Outline each Trypanosoma brucei.
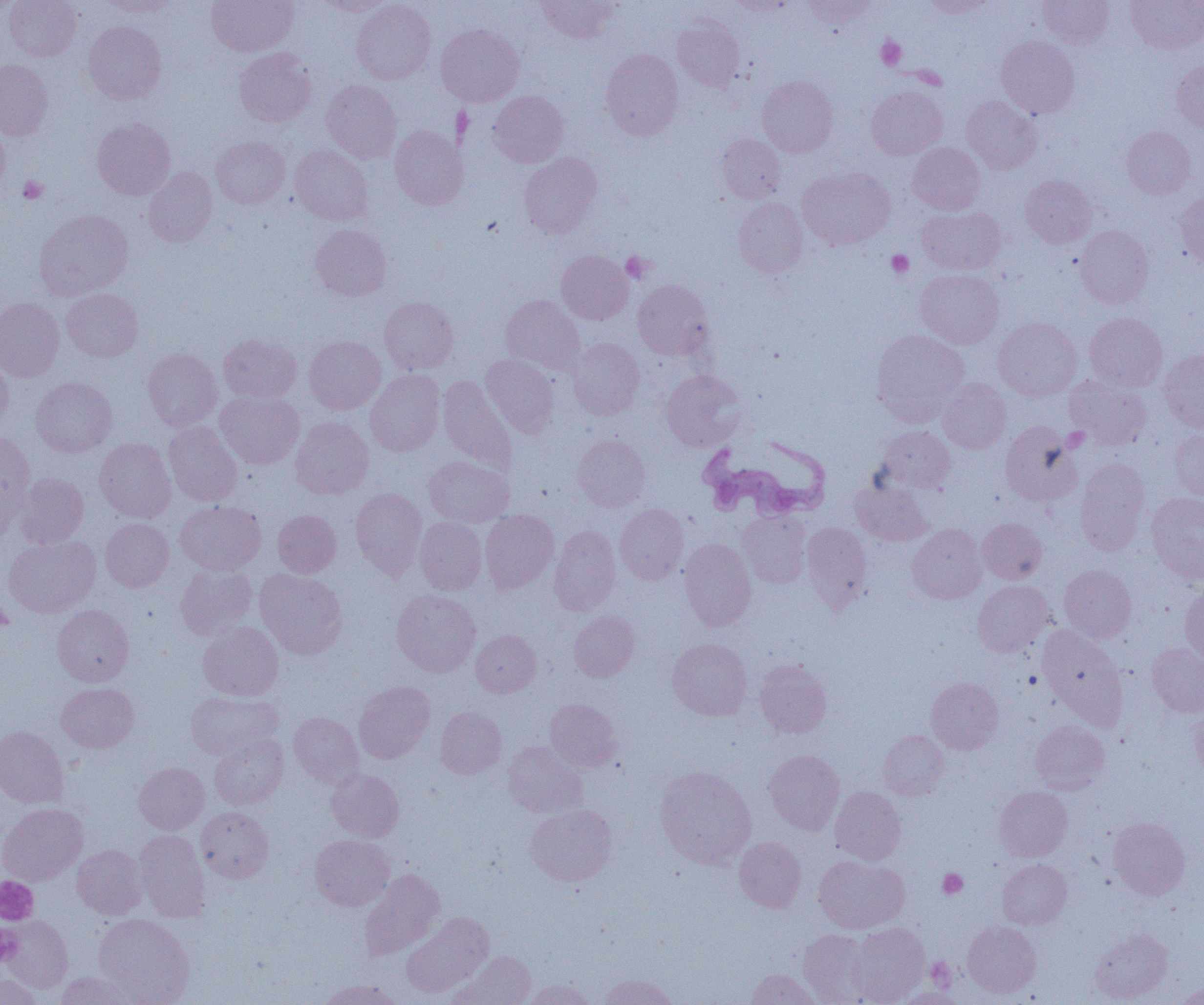

Approximate bounding boxes as named x1/y1/x2/y2 corners in pixels.
Trypanosoma brucei: (x1=698, y1=434, x2=830, y2=523).

Summary:
  - Platelet locations: (x1=877, y1=37, x2=906, y2=70), (x1=19, y1=175, x2=48, y2=203), (x1=886, y1=250, x2=913, y2=277), (x1=622, y1=252, x2=654, y2=283), (x1=938, y1=868, x2=967, y2=899), (x1=0, y1=877, x2=37, y2=923), (x1=0, y1=926, x2=22, y2=965), (x1=925, y1=957, x2=956, y2=990)
  - Uninfected red blood cell locations: (x1=4, y1=0, x2=80, y2=61), (x1=206, y1=0, x2=299, y2=56), (x1=316, y1=0, x2=395, y2=16), (x1=351, y1=0, x2=435, y2=85), (x1=535, y1=0, x2=619, y2=42), (x1=726, y1=0, x2=796, y2=17), (x1=802, y1=0, x2=877, y2=28), (x1=919, y1=0, x2=995, y2=18), (x1=1037, y1=0, x2=1114, y2=48), (x1=1126, y1=0, x2=1204, y2=53), (x1=0, y1=1, x2=17, y2=18), (x1=98, y1=1, x2=181, y2=16), (x1=672, y1=17, x2=744, y2=91), (x1=83, y1=21, x2=167, y2=105), (x1=436, y1=24, x2=524, y2=106), (x1=996, y1=35, x2=1079, y2=118), (x1=234, y1=47, x2=316, y2=127), (x1=600, y1=49, x2=683, y2=140), (x1=0, y1=59, x2=54, y2=140), (x1=1172, y1=60, x2=1204, y2=131), (x1=757, y1=75, x2=838, y2=157), (x1=322, y1=80, x2=402, y2=163), (x1=866, y1=86, x2=948, y2=159), (x1=488, y1=90, x2=568, y2=167), (x1=962, y1=96, x2=1042, y2=173), (x1=92, y1=118, x2=175, y2=200), (x1=0, y1=119, x2=10, y2=194), (x1=390, y1=126, x2=468, y2=210), (x1=1122, y1=126, x2=1196, y2=198), (x1=717, y1=133, x2=786, y2=203), (x1=211, y1=136, x2=290, y2=209), (x1=908, y1=143, x2=985, y2=214), (x1=290, y1=144, x2=373, y2=225), (x1=519, y1=152, x2=602, y2=238), (x1=143, y1=167, x2=217, y2=247), (x1=797, y1=167, x2=895, y2=249), (x1=1020, y1=175, x2=1096, y2=247), (x1=1176, y1=192, x2=1204, y2=269), (x1=733, y1=197, x2=808, y2=277), (x1=917, y1=206, x2=1006, y2=275), (x1=35, y1=209, x2=133, y2=300), (x1=310, y1=224, x2=391, y2=300), (x1=1075, y1=225, x2=1153, y2=308), (x1=556, y1=251, x2=633, y2=324), (x1=915, y1=269, x2=1003, y2=348), (x1=633, y1=279, x2=714, y2=360), (x1=61, y1=288, x2=143, y2=361), (x1=501, y1=295, x2=585, y2=376), (x1=379, y1=297, x2=459, y2=374), (x1=0, y1=298, x2=65, y2=381), (x1=1085, y1=313, x2=1167, y2=392), (x1=993, y1=317, x2=1081, y2=401), (x1=872, y1=330, x2=968, y2=423), (x1=218, y1=334, x2=301, y2=403), (x1=304, y1=335, x2=385, y2=414), (x1=567, y1=337, x2=645, y2=419), (x1=143, y1=348, x2=222, y2=431), (x1=1158, y1=349, x2=1204, y2=433), (x1=481, y1=354, x2=559, y2=438), (x1=0, y1=355, x2=13, y2=431), (x1=366, y1=369, x2=445, y2=456), (x1=661, y1=369, x2=745, y2=451), (x1=1065, y1=375, x2=1152, y2=450), (x1=438, y1=376, x2=517, y2=474), (x1=30, y1=377, x2=117, y2=457), (x1=937, y1=378, x2=1011, y2=454), (x1=215, y1=391, x2=305, y2=468), (x1=291, y1=416, x2=374, y2=499), (x1=164, y1=420, x2=242, y2=507), (x1=1000, y1=421, x2=1082, y2=506), (x1=877, y1=426, x2=956, y2=493), (x1=1170, y1=429, x2=1204, y2=502), (x1=0, y1=432, x2=35, y2=527), (x1=572, y1=434, x2=650, y2=511), (x1=94, y1=438, x2=176, y2=522), (x1=424, y1=456, x2=514, y2=527), (x1=1075, y1=459, x2=1151, y2=555), (x1=15, y1=473, x2=89, y2=548), (x1=852, y1=480, x2=932, y2=546), (x1=350, y1=487, x2=427, y2=580), (x1=1146, y1=492, x2=1204, y2=582), (x1=175, y1=501, x2=266, y2=575), (x1=615, y1=504, x2=689, y2=584), (x1=273, y1=510, x2=341, y2=577), (x1=480, y1=510, x2=559, y2=593), (x1=738, y1=511, x2=811, y2=587), (x1=415, y1=517, x2=487, y2=595), (x1=101, y1=518, x2=174, y2=591), (x1=977, y1=518, x2=1047, y2=584), (x1=801, y1=522, x2=872, y2=611), (x1=907, y1=524, x2=987, y2=604), (x1=549, y1=526, x2=621, y2=615), (x1=4, y1=535, x2=100, y2=618), (x1=678, y1=538, x2=756, y2=630), (x1=175, y1=563, x2=257, y2=639), (x1=1059, y1=565, x2=1136, y2=642), (x1=255, y1=568, x2=348, y2=659), (x1=972, y1=580, x2=1055, y2=657), (x1=1180, y1=586, x2=1204, y2=661), (x1=392, y1=589, x2=481, y2=676), (x1=53, y1=605, x2=133, y2=687), (x1=568, y1=611, x2=640, y2=682), (x1=198, y1=622, x2=284, y2=701), (x1=1038, y1=626, x2=1124, y2=719), (x1=471, y1=630, x2=541, y2=697), (x1=667, y1=638, x2=752, y2=720), (x1=1146, y1=643, x2=1204, y2=716), (x1=754, y1=659, x2=832, y2=738), (x1=926, y1=677, x2=1003, y2=753), (x1=353, y1=681, x2=435, y2=763), (x1=56, y1=683, x2=139, y2=753), (x1=186, y1=691, x2=282, y2=761), (x1=545, y1=698, x2=621, y2=772), (x1=1189, y1=704, x2=1204, y2=776), (x1=435, y1=707, x2=507, y2=779), (x1=289, y1=712, x2=364, y2=787), (x1=1030, y1=721, x2=1109, y2=794), (x1=0, y1=726, x2=69, y2=808), (x1=879, y1=730, x2=950, y2=800), (x1=209, y1=733, x2=288, y2=809), (x1=502, y1=742, x2=587, y2=818), (x1=764, y1=749, x2=844, y2=834), (x1=134, y1=762, x2=209, y2=833), (x1=655, y1=766, x2=756, y2=868), (x1=326, y1=768, x2=404, y2=842), (x1=994, y1=786, x2=1072, y2=862), (x1=830, y1=787, x2=905, y2=864), (x1=0, y1=803, x2=88, y2=886), (x1=525, y1=804, x2=616, y2=886), (x1=197, y1=807, x2=273, y2=882), (x1=1108, y1=817, x2=1190, y2=899), (x1=134, y1=830, x2=209, y2=922), (x1=309, y1=834, x2=394, y2=911), (x1=734, y1=836, x2=806, y2=912), (x1=72, y1=845, x2=146, y2=919), (x1=814, y1=855, x2=910, y2=934), (x1=997, y1=859, x2=1071, y2=929), (x1=360, y1=869, x2=444, y2=961), (x1=401, y1=912, x2=493, y2=998), (x1=94, y1=913, x2=195, y2=1004), (x1=1, y1=916, x2=73, y2=993), (x1=963, y1=921, x2=1041, y2=998), (x1=849, y1=922, x2=930, y2=1005), (x1=798, y1=928, x2=878, y2=1004), (x1=1089, y1=929, x2=1172, y2=1003), (x1=451, y1=951, x2=536, y2=1005), (x1=746, y1=969, x2=822, y2=1005), (x1=57, y1=972, x2=137, y2=1005), (x1=0, y1=973, x2=42, y2=1005), (x1=598, y1=974, x2=677, y2=1005), (x1=320, y1=979, x2=400, y2=1005), (x1=523, y1=979, x2=596, y2=1005), (x1=1177, y1=983, x2=1204, y2=1004), (x1=895, y1=988, x2=966, y2=1005)
  - Slide-level diagnosis: Trypanosoma brucei
  - Modality: light microscopy
  - Image size: 1204×1005 pixels
  - Magnification: 1000x
  - Field of view: single
  - Preparation: thin blood smear